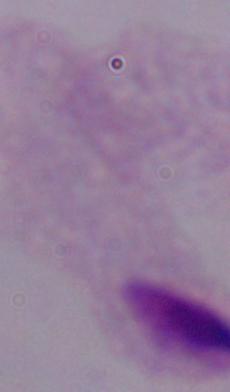

A trichomonad is shown. 1000x magnification. Photomicrograph.